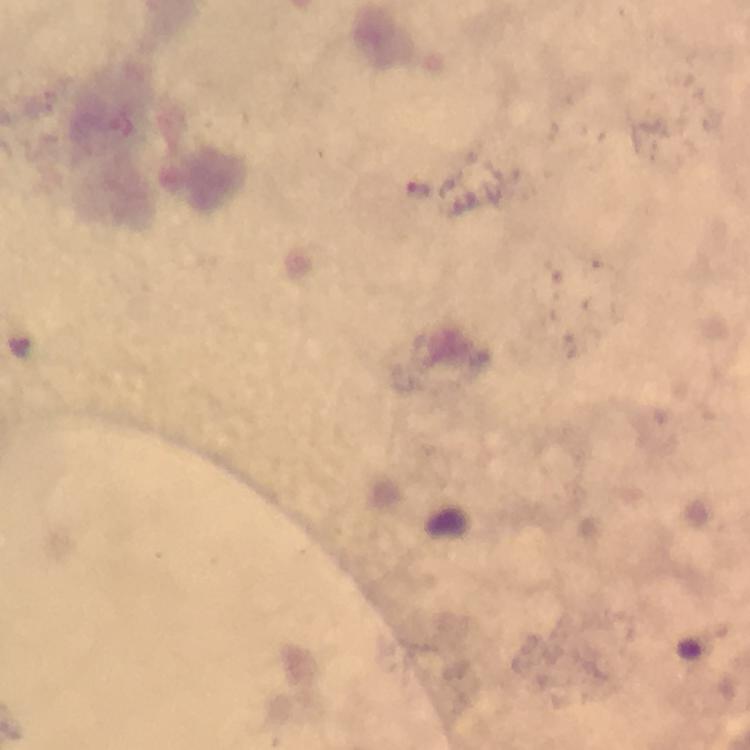

{
  "cropped_from": "a single field of view",
  "context": "from a diagnostic examination for malaria",
  "preparation": "thick blood smear",
  "magnification": "100x",
  "capture": "smartphone photograph through a microscope",
  "stain": "Giemsa",
  "plasmodium_parasite_locations": "approximate object centers, in pixels from the top-left corner: (x=419, y=194)",
  "image_size": "750×750 pixels",
  "immersion_oil": "used"
}